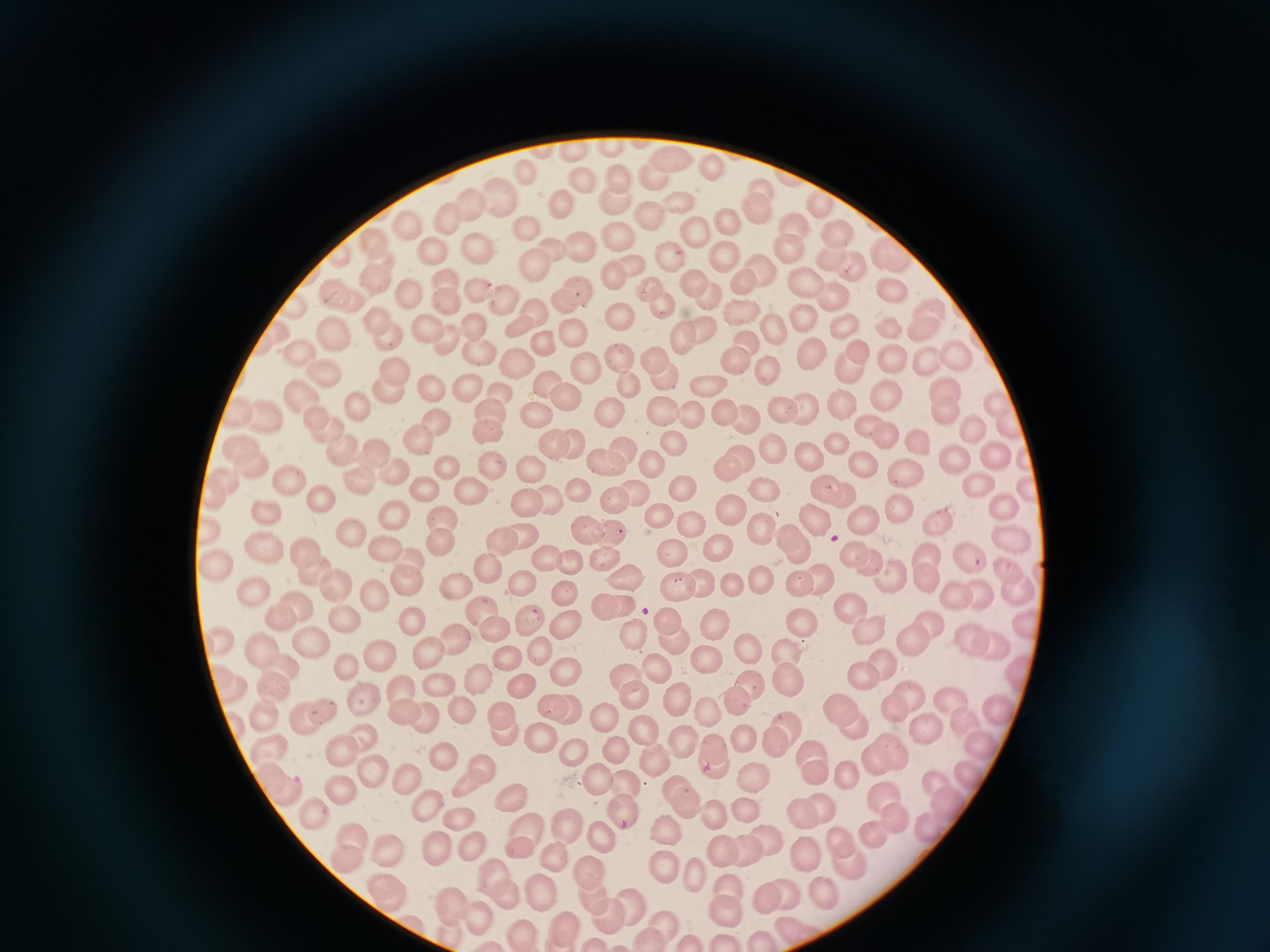

cell locations = approximate centers as (x, y) in pixels: (576, 151), (670, 160), (715, 167), (655, 172), (527, 173), (619, 173), (579, 177), (761, 186), (500, 195), (680, 198), (472, 204), (824, 204), (616, 205), (563, 206), (753, 208), (448, 216), (649, 218), (726, 220), (795, 220), (410, 225), (692, 227), (529, 228), (621, 234), (836, 235), (373, 241), (579, 245), (481, 246), (786, 246), (554, 247), (893, 255), (433, 257), (666, 258), (723, 259), (831, 260), (533, 261), (384, 264), (633, 264), (852, 266), (764, 269), (615, 275), (445, 278), (805, 278), (376, 281), (696, 284), (743, 284), (649, 287), (892, 289), (478, 292), (580, 292), (346, 295), (412, 296), (707, 296), (837, 296), (506, 299), (446, 301), (563, 303), (658, 303), (296, 307), (933, 307), (537, 312), (625, 313), (803, 320), (380, 321), (429, 323), (473, 325), (524, 325), (843, 325), (923, 328), (771, 329), (683, 330), (706, 330), (336, 335), (386, 336), (575, 336), (446, 338), (746, 340), (542, 344), (477, 349), (809, 350), (852, 351), (617, 355), (301, 356), (655, 358), (927, 358), (958, 358), (892, 359), (735, 360), (514, 363), (849, 366), (393, 367), (587, 367), (766, 374), (325, 375), (663, 377), (549, 383), (467, 384), (632, 385), (708, 386), (500, 389), (388, 390), (435, 390), (948, 391), (885, 394), (303, 395), (568, 397), (840, 401), (997, 401), (359, 405), (807, 407), (490, 409), (663, 409), (722, 409), (780, 409), (942, 410), (693, 412), (265, 413), (608, 413), (241, 414), (316, 415), (536, 418), (745, 418), (438, 419), (1007, 422), (870, 424), (971, 428), (333, 429), (487, 430), (882, 437), (418, 440), (575, 440), (837, 443), (676, 444), (918, 444), (552, 446), (242, 447), (345, 447), (621, 450), (774, 450), (373, 453), (811, 455), (991, 456), (953, 458), (737, 460), (655, 462), (606, 463), (864, 465), (246, 467), (445, 467), (493, 468), (531, 469), (905, 470), (395, 473), (288, 478), (356, 480), (976, 483), (682, 486), (825, 486), (223, 487), (467, 487), (1030, 487), (423, 489), (768, 491), (638, 492), (578, 494), (841, 495), (320, 499), (550, 500), (616, 502), (528, 503), (1001, 503), (902, 510), (731, 511), (263, 514), (659, 515), (861, 519), (400, 520), (817, 520), (939, 521), (442, 522), (690, 525), (583, 528), (211, 529), (761, 531), (526, 532), (607, 536), (791, 536), (355, 537), (1010, 537), (501, 541), (718, 546), (437, 547), (258, 550), (386, 550), (799, 551), (306, 554), (928, 555), (671, 556), (965, 556), (407, 557), (548, 559), (605, 559), (860, 559), (571, 564), (487, 565), (213, 566), (1006, 566), (309, 571), (892, 571), (928, 575), (625, 576), (406, 579), (796, 580), (817, 580), (762, 581), (519, 584), (702, 585), (455, 586), (734, 587), (335, 588), (678, 588), (1015, 590), (254, 591), (982, 591), (567, 594), (958, 595), (377, 599), (298, 605), (612, 605), (854, 606), (482, 609), (529, 617), (411, 618), (668, 619), (277, 620), (343, 620), (797, 621), (929, 625), (566, 626), (868, 626), (495, 628), (714, 628), (1023, 628), (632, 632), (670, 638), (218, 639), (455, 640), (969, 640), (912, 642), (993, 644), (312, 646), (261, 648), (542, 649), (426, 650), (750, 652), (791, 652), (379, 656), (504, 657), (707, 660), (880, 664), (658, 666), (284, 668), (865, 669), (347, 670), (567, 672), (1017, 674), (626, 676), (476, 679), (790, 682), (439, 683), (521, 685), (272, 686), (229, 688), (401, 692), (631, 694), (909, 694), (746, 697), (364, 700), (679, 702), (950, 702), (893, 707), (561, 708), (460, 709), (322, 712), (405, 713), (709, 713), (998, 713), (263, 714), (502, 715), (603, 715), (424, 716), (848, 718), (302, 721), (967, 722), (646, 725), (924, 728), (505, 733), (783, 735), (542, 736), (364, 738), (747, 739), (978, 741), (683, 745), (345, 748), (575, 749), (620, 750), (267, 752), (883, 753), (444, 755), (714, 756), (654, 760), (813, 763), (370, 769), (846, 771), (971, 772), (477, 773), (404, 776), (599, 776), (753, 778), (627, 782), (277, 790), (341, 790), (942, 796), (680, 802), (425, 804), (888, 806), (312, 809), (747, 811), (808, 812), (624, 813), (712, 816), (456, 820), (568, 825), (929, 827), (529, 831), (666, 831), (874, 835), (601, 836), (352, 838), (766, 838), (520, 846), (469, 848), (745, 849), (388, 850), (436, 850), (726, 850), (845, 851), (809, 855), (345, 856), (555, 864), (664, 868), (590, 874), (497, 875), (692, 876), (542, 888), (386, 890), (824, 893), (593, 895), (773, 895), (726, 896), (509, 897), (629, 900), (457, 907), (606, 914), (476, 920), (662, 923), (791, 927), (566, 928), (646, 941), (764, 941)
capture = smartphone camera at the microscope eyepiece
image size = 1270×952 pixels
stain = Giemsa
preparation = thin blood film
field of view = single